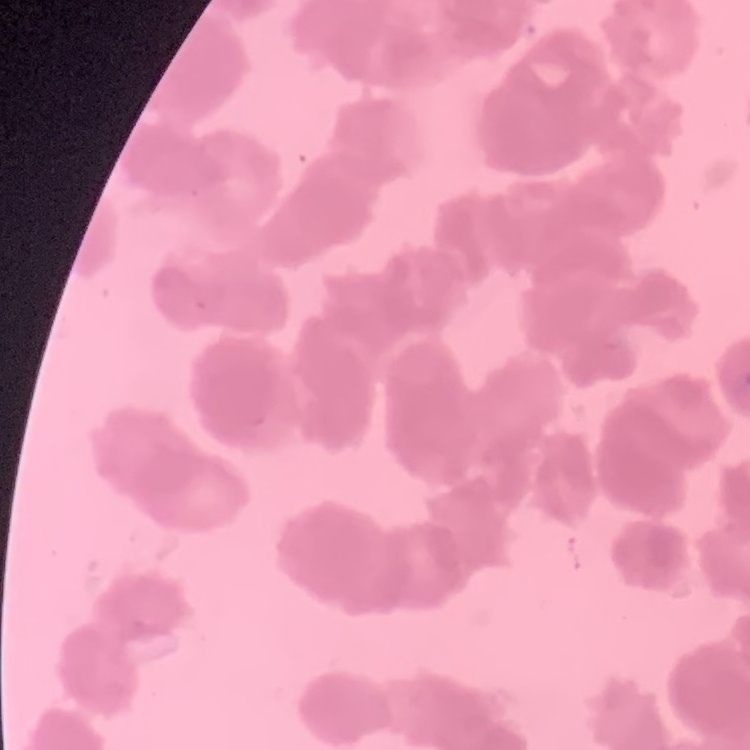

red blood cell morphology = rouleaux formation
stain = Field's or Giemsa
image type = square crop of a larger photomicrograph
preparation = thin blood film